Comment on the morphology of the red blood cells.
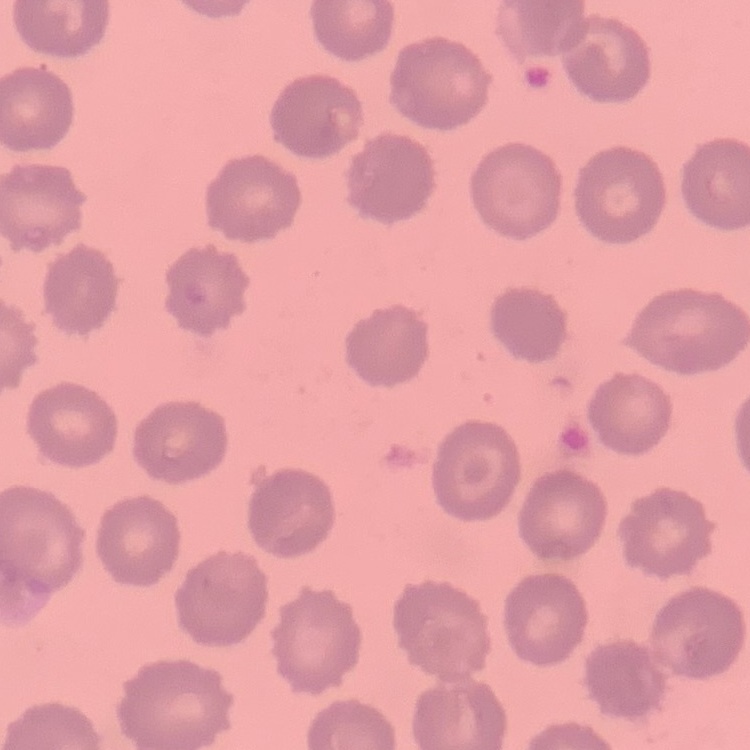
They show no rouleaux formation.

Stained with either Field's or Giemsa. Thin blood smear. One tile cut from a larger photomicrograph.